Identify the cell.
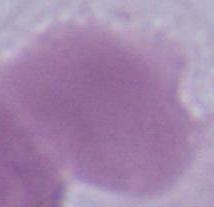
This is an erythrocyte.

modality = photomicrograph
magnification = 1000x